State the preparation type.
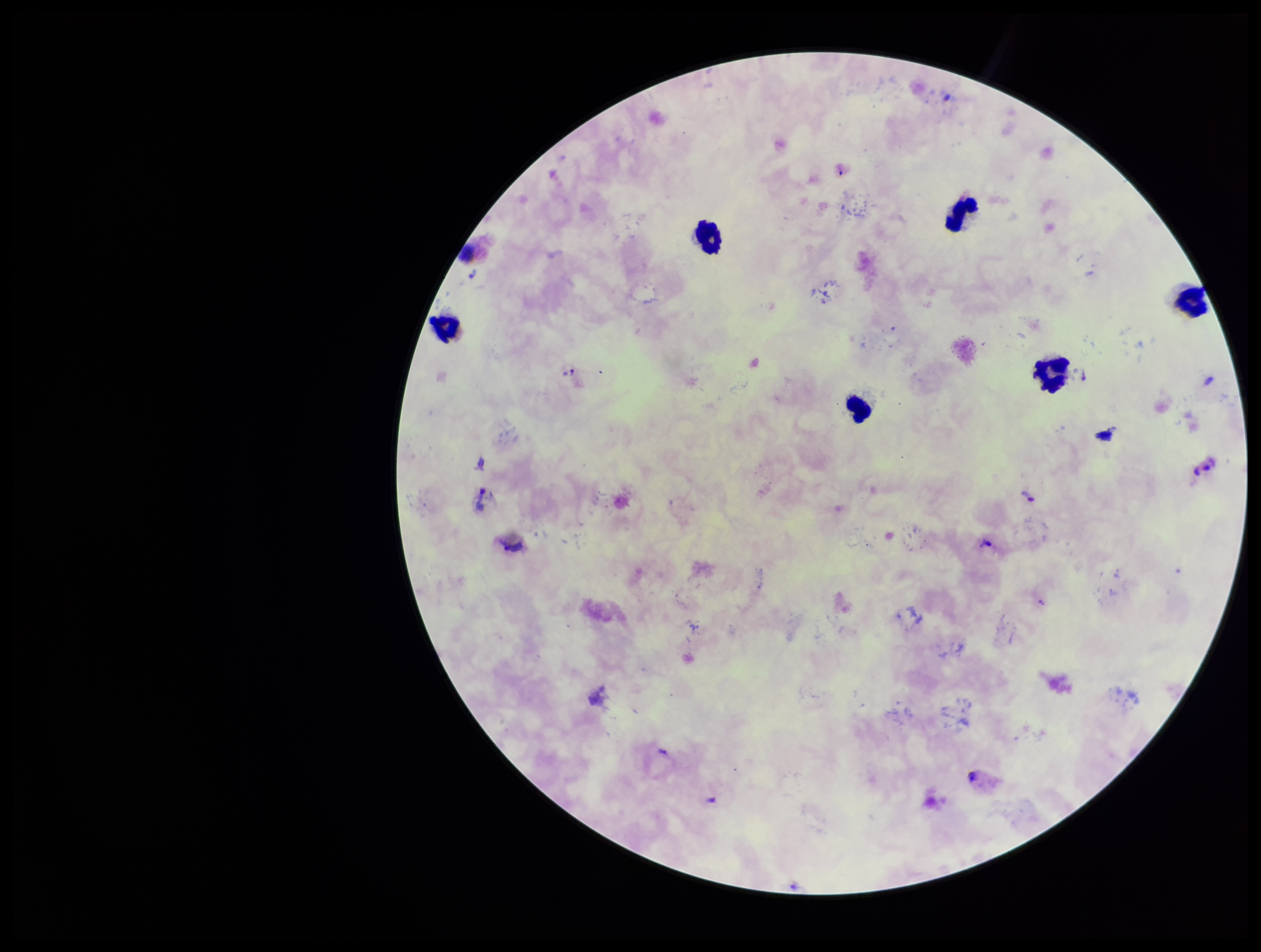

Thick.

Parasite count: 7. Image is 1261×952 pixels. One field from this slide. Smartphone photograph taken through the eyepiece of a microscope. Species reported for this patient: Plasmodium vivax. Giemsa stain. Leukocyte count: 7. Patient malaria status: positive. Plasmodium parasites: identified.